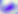 Micrograph. 400x magnification. Toxoplasma gondii is seen.